Name the parasite shown.
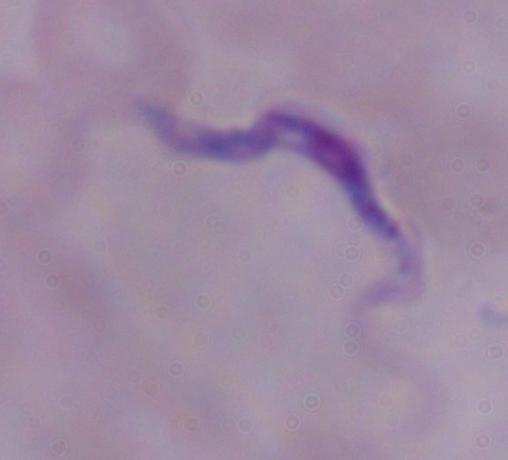
A trypanosome.

{
  "modality": "photomicrograph",
  "magnification": "1000x"
}